Report the malaria status of this cell.
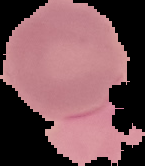
It is uninfected.

Image is 145×166 pixels. Cell region segmented out of the field of view; the surrounding area is masked to black. From a thin blood film.